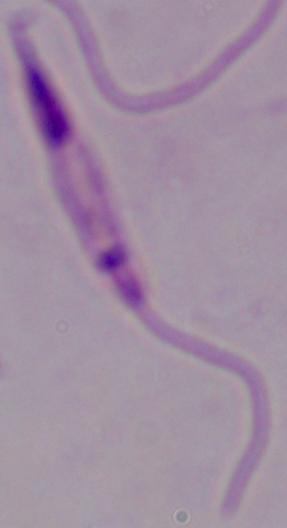
Captured at 1000x magnification. A Leishmania parasite is shown. Photomicrograph.